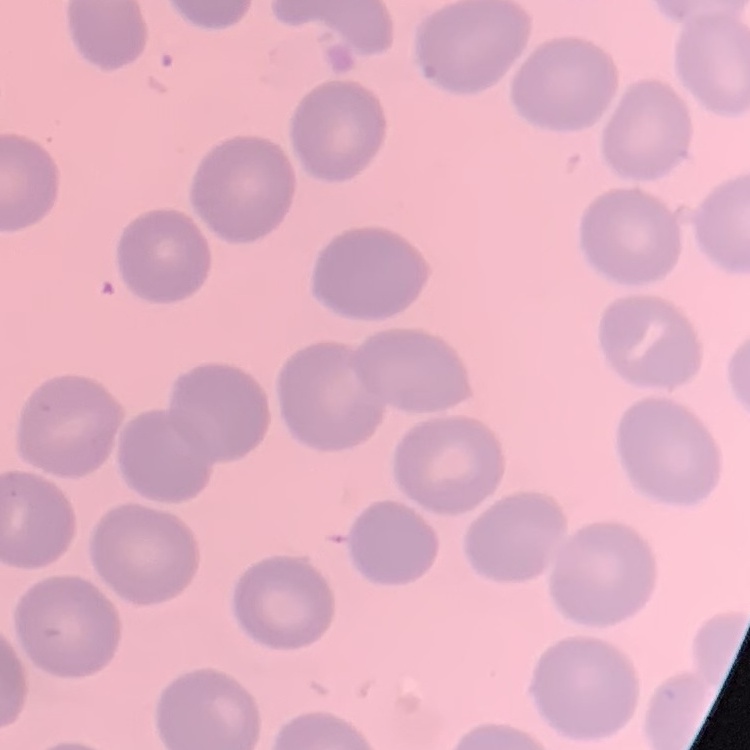 The red blood cells exhibit no rouleaux formation. Thin blood smear. One tile cut from a larger photomicrograph. Field's or Giemsa stain.